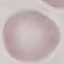
Result: negative for malaria parasites. Automatically extracted cell patch, resized to 64 × 64 pixels. Thin blood film. Photographed with a smartphone camera at the microscope eyepiece. Giemsa-stained preparation.